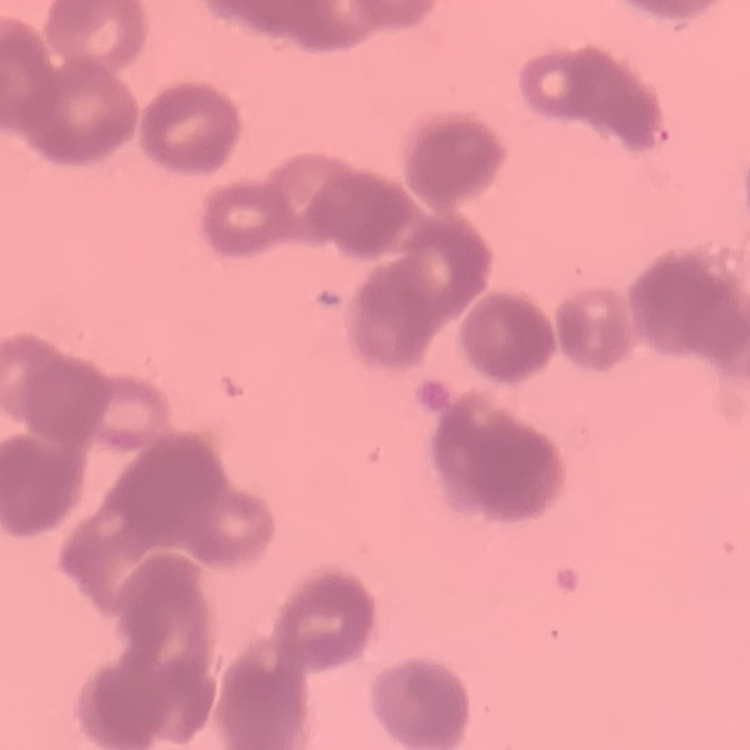
Summary:
  - Red blood cell morphology: rouleaux formation
  - Image type: square crop of a larger photomicrograph
  - Stain: Field's or Giemsa
  - Preparation: thin blood smear